Locate every uninfected red blood cell.
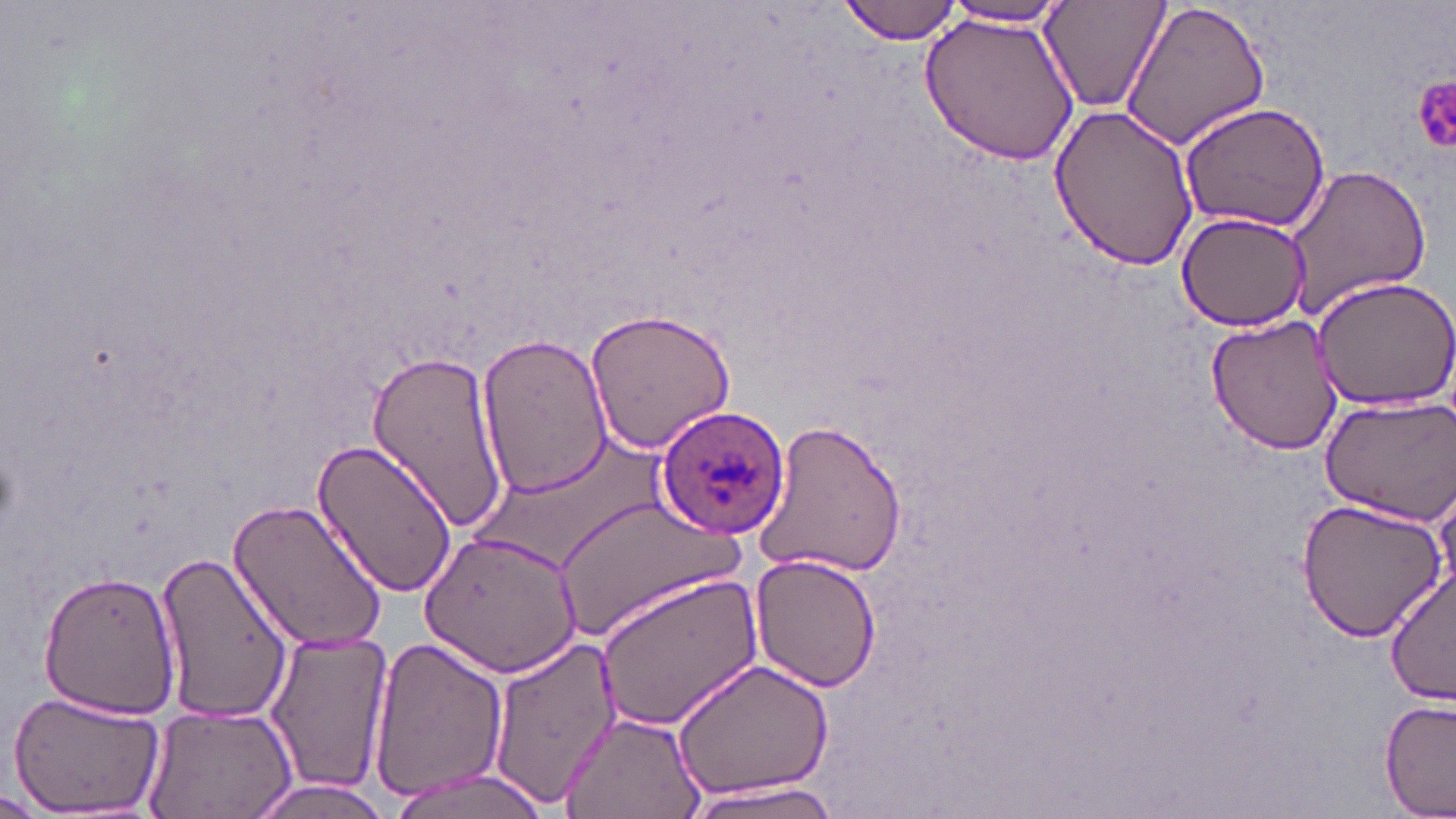
Approximate bounding boxes as (x1, y1, x2, y2) in pixels.
Uninfected red blood cells: (839, 0, 964, 44), (1120, 0, 1271, 152), (1040, 1, 1168, 111), (938, 2, 1074, 29), (920, 8, 1078, 166), (1047, 103, 1201, 270), (1179, 103, 1330, 232), (1281, 163, 1431, 319), (1174, 210, 1312, 332), (1308, 276, 1456, 411), (584, 306, 737, 457), (1208, 315, 1344, 455), (476, 333, 613, 501), (364, 351, 514, 532), (1317, 394, 1456, 525), (754, 415, 908, 582), (311, 437, 458, 598), (1294, 496, 1448, 642), (230, 497, 388, 654), (556, 498, 745, 639), (421, 529, 584, 679), (155, 550, 293, 724), (749, 551, 880, 693), (1385, 568, 1456, 707), (38, 569, 182, 722), (592, 571, 765, 734), (263, 631, 393, 799), (368, 636, 508, 806), (485, 638, 620, 806), (670, 657, 836, 804), (9, 691, 165, 814), (1379, 697, 1454, 818), (140, 704, 299, 819), (560, 709, 709, 819), (383, 768, 553, 819), (244, 777, 399, 819), (679, 780, 846, 817), (0, 789, 50, 817).

slide-level diagnosis = Plasmodium ovale
modality = optical microscopy
preparation = thin blood smear
field of view = single
platelet locations = approximate bounding boxes as (x1, y1, x2, y2) in pixels: (1412, 72, 1455, 156)
stain = May-Grünwald-Giemsa
magnification = 1000x
Plasmodium ovale-infected red blood cell locations = approximate bounding boxes as (x1, y1, x2, y2) in pixels: (653, 404, 789, 540)
image size = 1456×819 pixels